State which parasite is depicted.
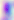

This is Toxoplasma gondii.

400x magnification. Photomicrograph.